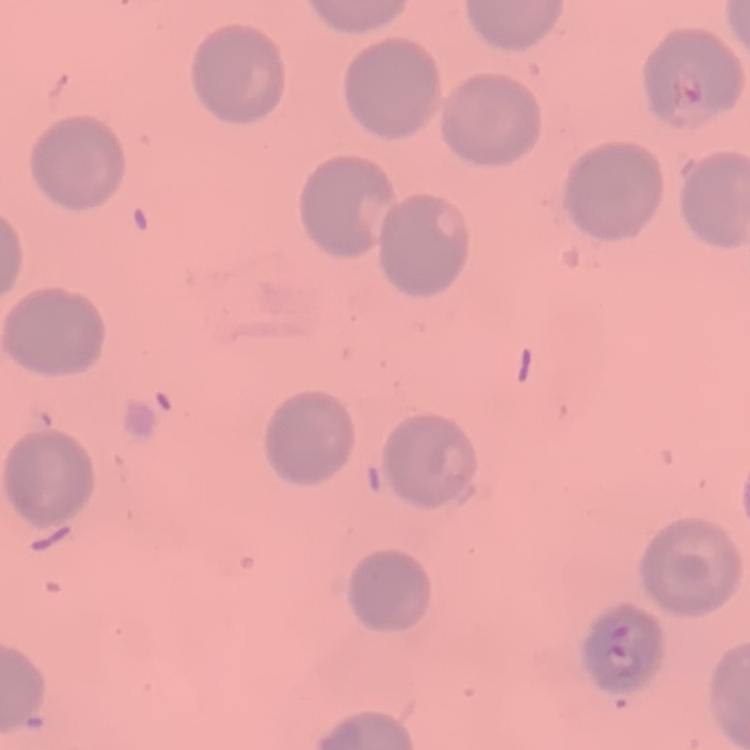

Summary:
  - Red blood cell morphology: no rouleaux formation
  - Image type: square crop of a larger photomicrograph
  - Preparation: thin peripheral smear
  - Stain: Field's or Giemsa